Classify this cell by malaria status.
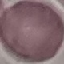
Uninfected.

Thin smear of blood. Giemsa-stained preparation. Cell patch, automatically extracted from a larger field of view and resized to 64 × 64 pixels. Photographed with a smartphone camera at the microscope eyepiece.